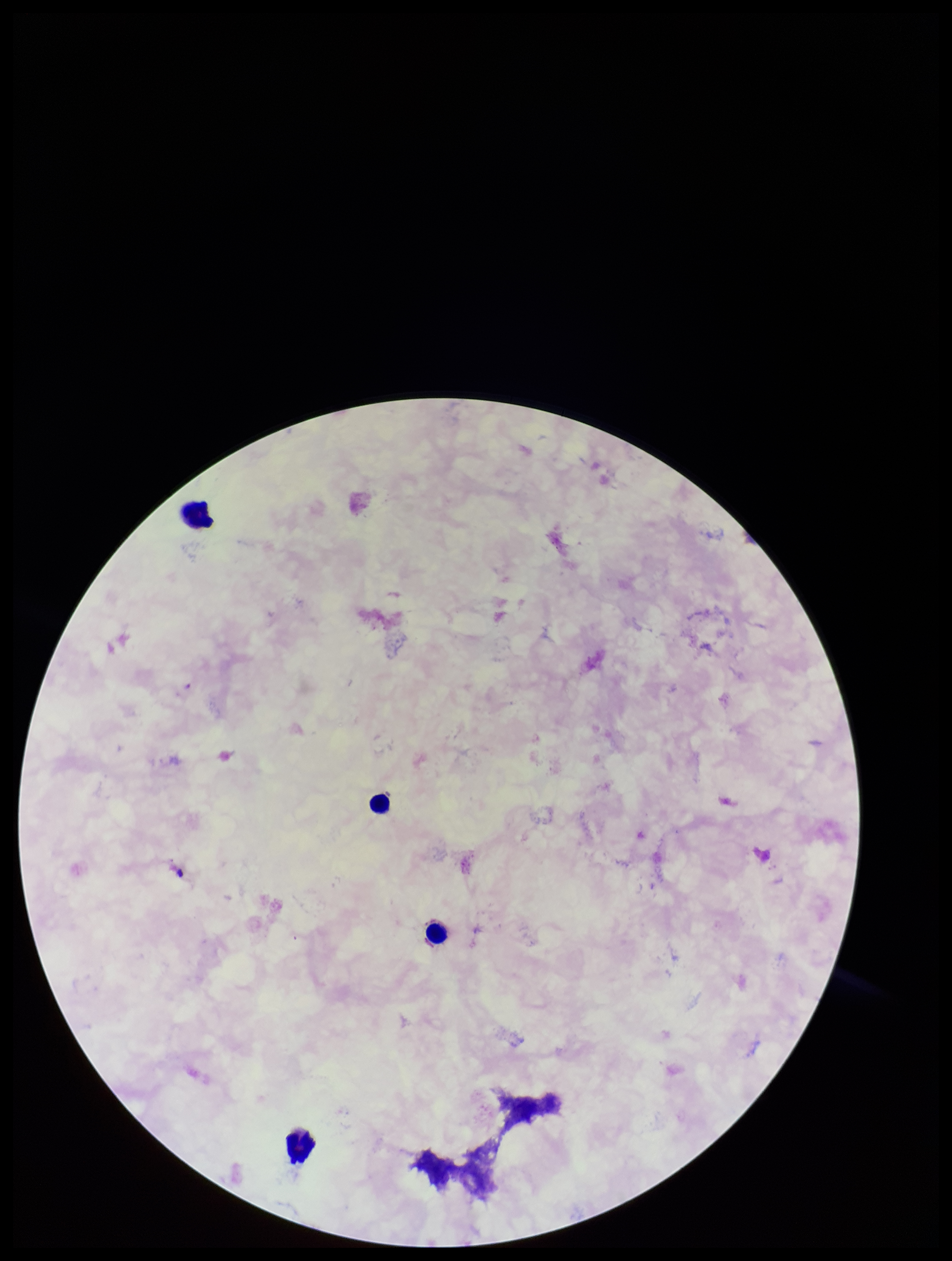 Preparation: thick blood smear. Stained with Giemsa. Plasmodium parasites: none identified. Photographed through the microscope eyepiece with a smartphone camera. Leukocyte count: 4. Single field of view. Species reported for this patient: Plasmodium falciparum. Image is 952×1261 pixels. Patient malaria status: positive. Parasite count: 0.